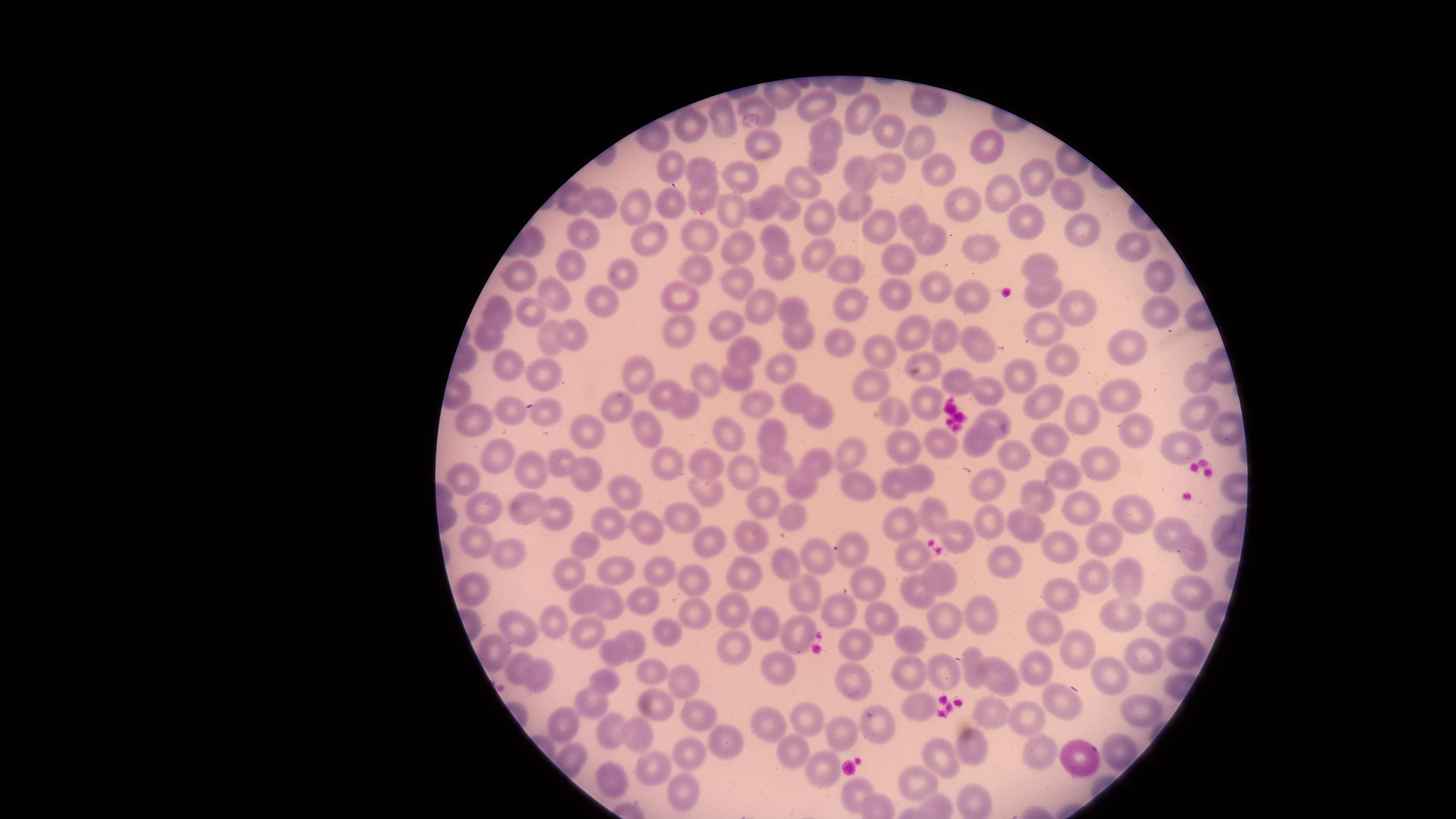

presence: no malaria parasites detected
image_size: 1456×819 pixels
visible_region: circular
uninfected_RBCs: 'approximate marker points, in pixels from the top-left corner: (x=818, y=102), (x=755, y=103), (x=926, y=105), (x=723, y=115), (x=858, y=115), (x=690, y=126), (x=826, y=129), (x=889, y=129), (x=920, y=143), (x=762, y=147), (x=989, y=148), (x=819, y=160), (x=673, y=163), (x=863, y=166), (x=887, y=166), (x=939, y=166), (x=699, y=171), (x=747, y=174), (x=1033, y=175), (x=806, y=182), (x=996, y=188), (x=1065, y=191), (x=695, y=196), (x=570, y=197), (x=854, y=199), (x=784, y=200), (x=668, y=202), (x=958, y=202), (x=642, y=208), (x=602, y=209), (x=763, y=209), (x=738, y=212), (x=819, y=214), (x=1025, y=218), (x=912, y=219), (x=879, y=223), (x=1077, y=228), (x=926, y=233), (x=590, y=234), (x=650, y=236), (x=700, y=236), (x=535, y=241), (x=777, y=241), (x=1134, y=248), (x=741, y=249), (x=983, y=249), (x=815, y=251), (x=898, y=258), (x=1037, y=260), (x=782, y=262), (x=572, y=264), (x=697, y=265), (x=621, y=271), (x=844, y=272), (x=525, y=273), (x=1159, y=278), (x=736, y=279), (x=932, y=284), (x=900, y=290), (x=1040, y=291), (x=553, y=295), (x=602, y=298), (x=686, y=300), (x=968, y=302), (x=762, y=303), (x=851, y=304), (x=1071, y=308), (x=1156, y=309), (x=497, y=310), (x=793, y=312), (x=529, y=314), (x=675, y=322), (x=1044, y=324), (x=728, y=326), (x=799, y=327), (x=568, y=332), (x=910, y=333), (x=547, y=335), (x=943, y=336), (x=490, y=337), (x=845, y=343), (x=983, y=343), (x=1127, y=349), (x=748, y=352), (x=883, y=354), (x=1057, y=355), (x=926, y=356), (x=773, y=359), (x=509, y=367), (x=549, y=372), (x=1194, y=373), (x=742, y=374), (x=1017, y=374), (x=643, y=375), (x=714, y=378), (x=961, y=378), (x=871, y=388), (x=665, y=390), (x=995, y=391), (x=792, y=394), (x=1119, y=397), (x=928, y=399), (x=1046, y=399), (x=680, y=404), (x=613, y=407), (x=818, y=407), (x=510, y=408), (x=757, y=408), (x=1194, y=408), (x=1085, y=411), (x=546, y=416), (x=993, y=416), (x=474, y=418), (x=892, y=419), (x=585, y=427), (x=1127, y=427), (x=767, y=429), (x=1221, y=430), (x=730, y=433), (x=1051, y=433), (x=978, y=436), (x=652, y=440), (x=900, y=444), (x=1184, y=446), (x=942, y=447), (x=1009, y=449), (x=851, y=452), (x=500, y=461), (x=709, y=462), (x=556, y=463), (x=821, y=463), (x=1094, y=463), (x=530, y=465), (x=667, y=466), (x=781, y=468), (x=1064, y=473), (x=584, y=476), (x=468, y=479), (x=744, y=480), (x=990, y=480), (x=917, y=481), (x=897, y=483), (x=856, y=486), (x=800, y=489), (x=709, y=493), (x=627, y=494), (x=1039, y=497), (x=769, y=500), (x=484, y=509), (x=526, y=509), (x=1081, y=509), (x=1135, y=509), (x=558, y=513), (x=939, y=513), (x=800, y=516), (x=905, y=520), (x=685, y=521), (x=616, y=523), (x=992, y=523), (x=1027, y=523), (x=1169, y=530), (x=649, y=531), (x=960, y=532), (x=759, y=536), (x=1105, y=537), (x=1058, y=540), (x=475, y=542), (x=709, y=547), (x=589, y=549), (x=852, y=551), (x=509, y=554), (x=818, y=556), (x=909, y=556), (x=1196, y=556), (x=1010, y=559), (x=787, y=568), (x=613, y=570), (x=745, y=571), (x=664, y=572), (x=1123, y=575), (x=577, y=576), (x=945, y=577), (x=1096, y=577), (x=875, y=578), (x=697, y=580), (x=478, y=591), (x=1186, y=592), (x=916, y=593), (x=1060, y=594), (x=810, y=595), (x=584, y=600), (x=607, y=601), (x=644, y=603), (x=695, y=613), (x=733, y=613), (x=1121, y=613), (x=984, y=614), (x=842, y=615), (x=1042, y=615), (x=1163, y=617), (x=878, y=618), (x=945, y=620), (x=511, y=625), (x=552, y=625), (x=661, y=626), (x=765, y=627), (x=590, y=632), (x=807, y=633), (x=918, y=641), (x=858, y=642), (x=637, y=643), (x=739, y=643), (x=1070, y=643), (x=496, y=651), (x=609, y=653), (x=1178, y=653), (x=1145, y=656), (x=777, y=662), (x=1046, y=667), (x=914, y=668), (x=515, y=669), (x=945, y=669), (x=648, y=671), (x=971, y=671), (x=1109, y=674), (x=996, y=678), (x=540, y=679), (x=605, y=679), (x=852, y=679), (x=691, y=681), (x=1056, y=699), (x=597, y=703), (x=656, y=706), (x=918, y=707), (x=1144, y=709), (x=693, y=713), (x=998, y=713), (x=1032, y=715), (x=804, y=719), (x=565, y=721), (x=877, y=724), (x=768, y=725), (x=607, y=728), (x=842, y=735), (x=640, y=736), (x=721, y=739), (x=969, y=746), (x=793, y=751), (x=1043, y=751), (x=1118, y=754), (x=688, y=756), (x=1076, y=761), (x=937, y=762), (x=659, y=764), (x=820, y=779), (x=920, y=779), (x=611, y=781), (x=674, y=788), (x=854, y=796)'
preparation: thin blood smear
stain: Giemsa
capture: smartphone photograph through the microscope eyepiece
field_of_view: single